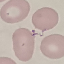
Malaria status: uninfected. Cell patch, automatically extracted from a larger field of view and resized to 64 × 64 pixels. Thin smear of blood. Giemsa stain. Photographed with a smartphone camera at the microscope eyepiece.